Locate and identify every blood parasite.
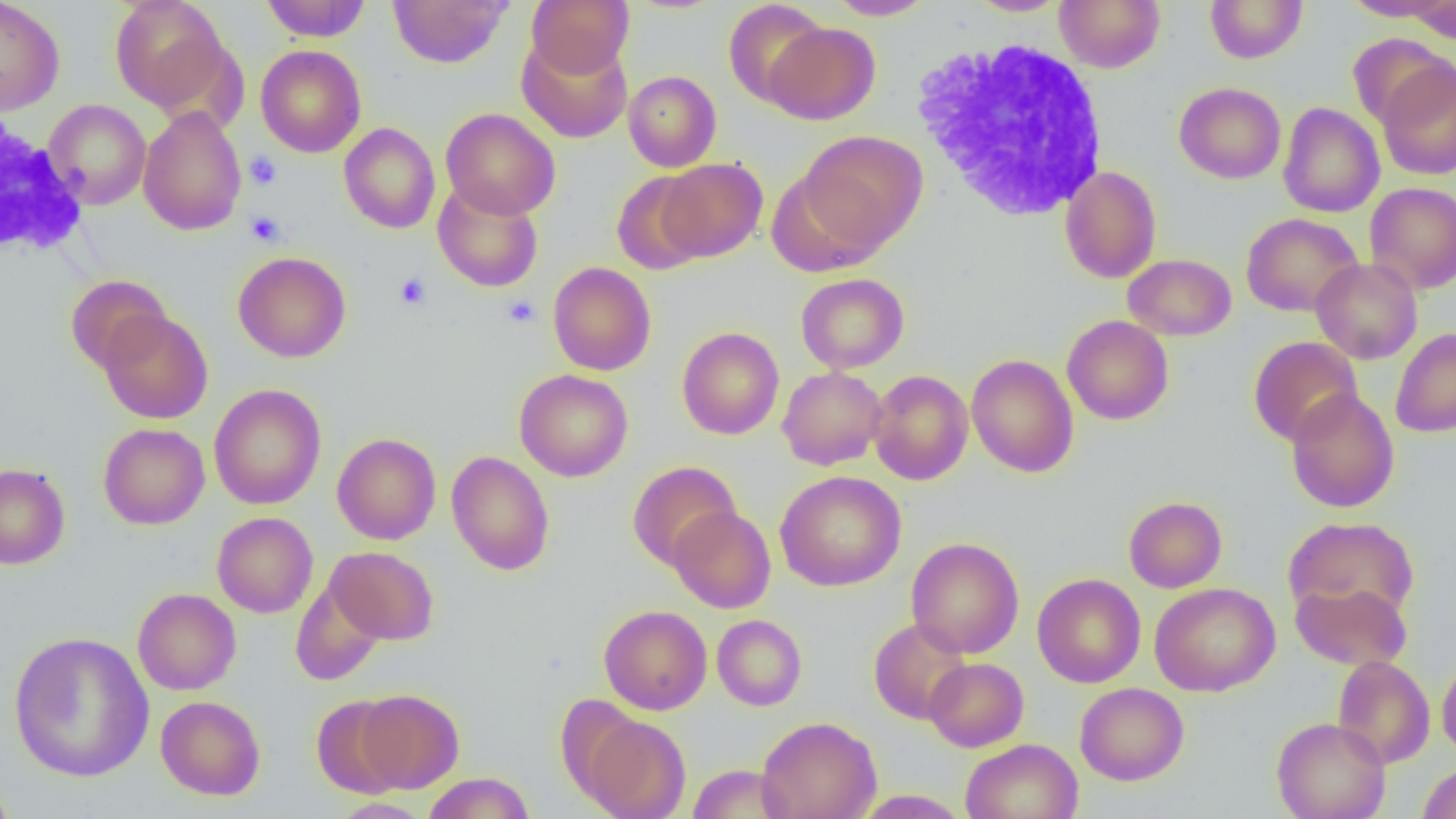
No blood parasites observed.

slide-level diagnosis = no evidence of blood parasites
modality = optical microscopy
platelet locations = approximate bounding boxes as (x1,y1)-(x2,y2) corner pairs in pixels: (245,152)-(282,190), (246,212)-(285,247), (394,272)-(431,310), (502,295)-(540,328)
magnification = 1000x
uninfected red blood cell locations = approximate bounding boxes as (x1,y1)-(x2,y2) corner pairs in pixels: (0,0)-(65,115), (110,0)-(231,113), (261,0)-(371,42), (388,0)-(512,68), (527,0)-(633,77), (825,0)-(936,20), (965,0)-(1070,16), (1054,0)-(1165,72), (1205,0)-(1307,63), (1340,0)-(1453,22), (723,1)-(829,107), (1406,1)-(1456,43), (765,22)-(880,125), (517,34)-(633,143), (1348,34)-(1453,130), (254,44)-(366,158), (1376,58)-(1456,180), (623,70)-(721,171), (1174,81)-(1286,183), (43,99)-(151,209), (1278,102)-(1385,218), (138,105)-(247,236), (440,108)-(560,220), (339,122)-(440,233), (798,130)-(927,253), (658,158)-(767,262), (1060,165)-(1162,283), (611,170)-(710,275), (433,181)-(544,292), (1364,182)-(1456,295), (1241,213)-(1363,316), (233,251)-(351,362), (1123,254)-(1236,341), (1311,258)-(1423,364), (547,262)-(656,376), (795,273)-(909,374), (65,275)-(172,374), (98,309)-(213,424), (1062,315)-(1174,425), (677,327)-(784,440), (1390,328)-(1456,437), (1248,336)-(1363,446), (966,354)-(1079,478), (777,366)-(887,470), (514,369)-(633,481), (869,369)-(974,485), (208,384)-(326,510), (1285,389)-(1399,513), (98,423)-(210,529), (331,432)-(441,545), (446,451)-(555,576), (628,461)-(741,570), (0,463)-(70,569), (775,470)-(906,592), (1124,496)-(1227,592), (668,506)-(776,613), (212,512)-(318,618), (1283,515)-(1419,623), (906,537)-(1024,658), (326,546)-(439,645), (1032,573)-(1146,688), (291,578)-(386,685), (1290,579)-(1413,671), (1150,582)-(1280,696), (132,588)-(241,695), (599,604)-(712,715), (712,614)-(807,710), (869,617)-(972,725), (9,631)-(154,782), (1437,654)-(1456,760), (1332,655)-(1435,768), (924,657)-(1028,752), (1075,682)-(1189,785), (355,688)-(464,792), (312,694)-(409,799), (156,695)-(265,799), (580,714)-(691,819), (756,716)-(882,819), (1271,716)-(1391,819), (961,738)-(1083,819), (1417,762)-(1456,818), (687,764)-(792,818), (0,767)-(16,819), (422,772)-(535,819), (854,790)-(970,818), (328,797)-(434,819)
field of view = one of a larger specimen
image size = 1456×819 pixels
white blood cell locations = approximate bounding boxes as (x1,y1)-(x2,y2) corner pairs in pixels: (911,37)-(1112,221), (0,112)-(88,261)
preparation = thin blood smear